Locate every uninfected red blood cell.
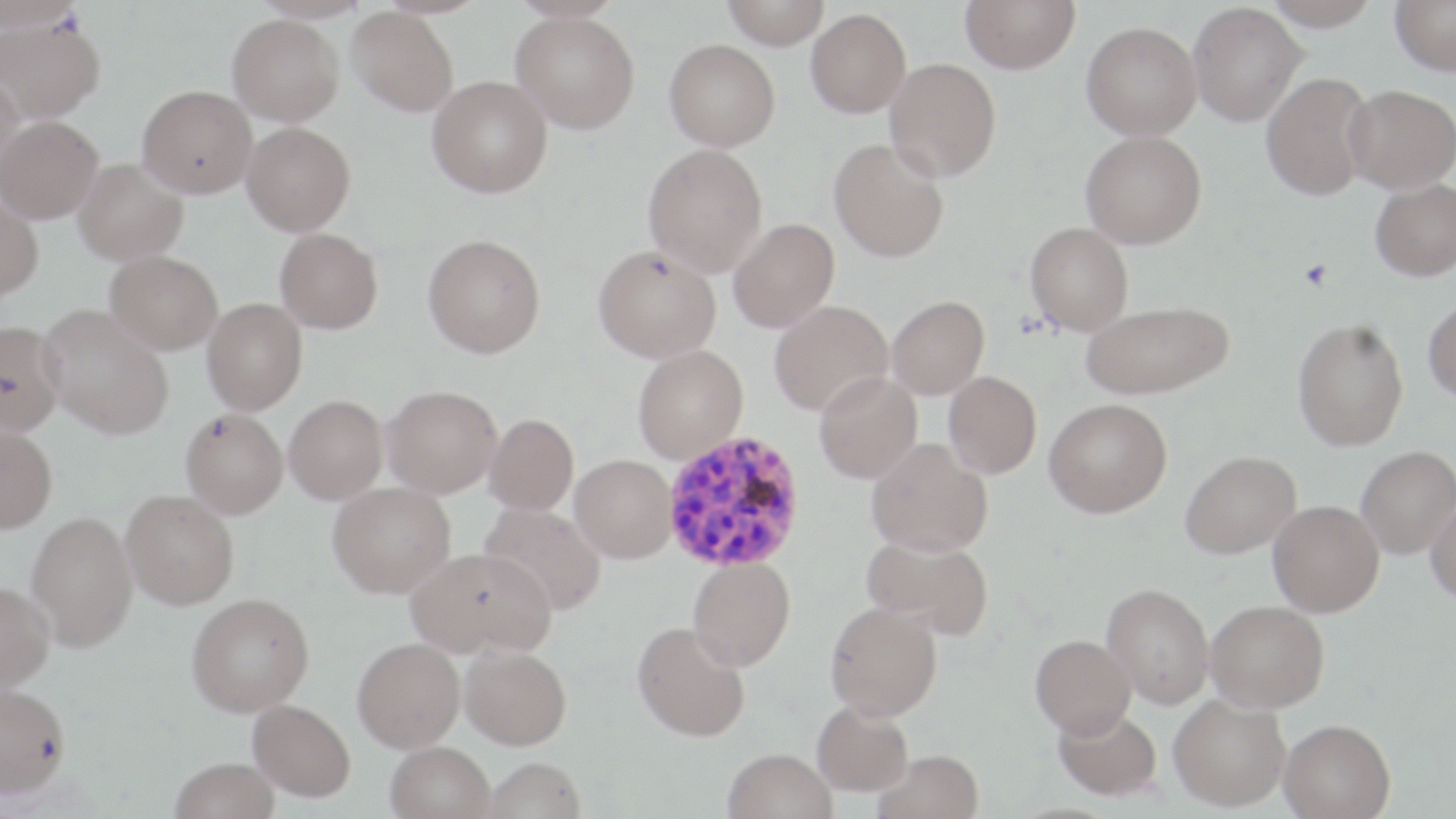
Approximate bounding boxes as [x1, y1, x2, y2] in pixels.
Uninfected red blood cells: [721, 0, 829, 49], [960, 0, 1080, 73], [1263, 0, 1382, 31], [1390, 0, 1456, 76], [0, 1, 80, 33], [1188, 2, 1306, 126], [347, 7, 458, 116], [806, 8, 911, 118], [511, 11, 640, 134], [0, 14, 105, 123], [227, 14, 344, 126], [1081, 21, 1202, 139], [664, 39, 780, 151], [884, 57, 1001, 181], [0, 69, 25, 180], [1261, 72, 1374, 200], [427, 75, 553, 198], [1343, 84, 1456, 194], [137, 85, 257, 198], [1, 116, 103, 223], [241, 122, 355, 236], [1080, 130, 1206, 249], [828, 138, 950, 263], [642, 143, 768, 277], [73, 158, 188, 265], [1370, 178, 1456, 282], [0, 198, 43, 301], [728, 218, 839, 332], [1025, 222, 1134, 335], [274, 227, 383, 334], [423, 234, 546, 359], [593, 244, 721, 363], [105, 250, 223, 355], [886, 295, 989, 399], [1423, 297, 1456, 404], [202, 298, 307, 415], [1082, 299, 1234, 399], [769, 300, 893, 416], [38, 305, 174, 440], [1292, 317, 1409, 451], [0, 321, 64, 437], [632, 344, 748, 464], [814, 371, 922, 483], [943, 371, 1041, 479], [382, 385, 502, 498], [284, 395, 388, 504], [1044, 398, 1172, 517], [180, 408, 288, 519], [484, 414, 579, 514], [0, 425, 57, 533], [866, 438, 992, 557], [1355, 445, 1456, 559], [1180, 450, 1301, 559], [570, 454, 676, 562], [328, 482, 456, 598], [120, 489, 239, 609], [1425, 497, 1456, 606], [1268, 500, 1384, 617], [479, 503, 607, 615], [26, 511, 138, 651], [861, 532, 994, 641], [406, 546, 556, 659], [687, 557, 795, 671], [0, 581, 54, 693], [1102, 583, 1215, 709], [186, 592, 315, 716], [1206, 600, 1330, 713], [825, 602, 943, 721], [632, 622, 751, 742], [1030, 634, 1137, 737], [352, 637, 465, 752], [459, 645, 572, 750], [0, 682, 70, 797], [1168, 694, 1291, 811], [248, 699, 355, 801], [812, 700, 914, 797], [1053, 705, 1162, 800], [1279, 718, 1396, 818], [385, 740, 495, 819], [723, 748, 837, 819], [875, 750, 984, 819], [170, 757, 280, 819], [483, 757, 587, 819].

{
  "slide_level_diagnosis": "Plasmodium vivax",
  "magnification": "1000x",
  "stain": "May-Grünwald-Giemsa",
  "field_of_view": "one of a larger specimen",
  "modality": "light microscopy",
  "preparation": "thin blood smear",
  "plasmodium_vivax_infected_red_blood_cell_locations": "approximate bounding boxes as [x1, y1, x2, y2] in pixels: [661, 430, 807, 574]",
  "image_size": "1456×819 pixels"
}